Assess this cell for malaria.
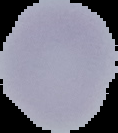

Uninfected.

{
  "preparation": "thin blood film",
  "image_type": "cell region segmented out of the field of view; surrounding area masked to black",
  "image_size": "118×133 pixels"
}